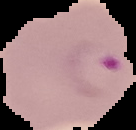

image_size: 136×130 pixels
result: malaria parasites detected
image_type: segmented cell region on a black background
preparation: thin blood film